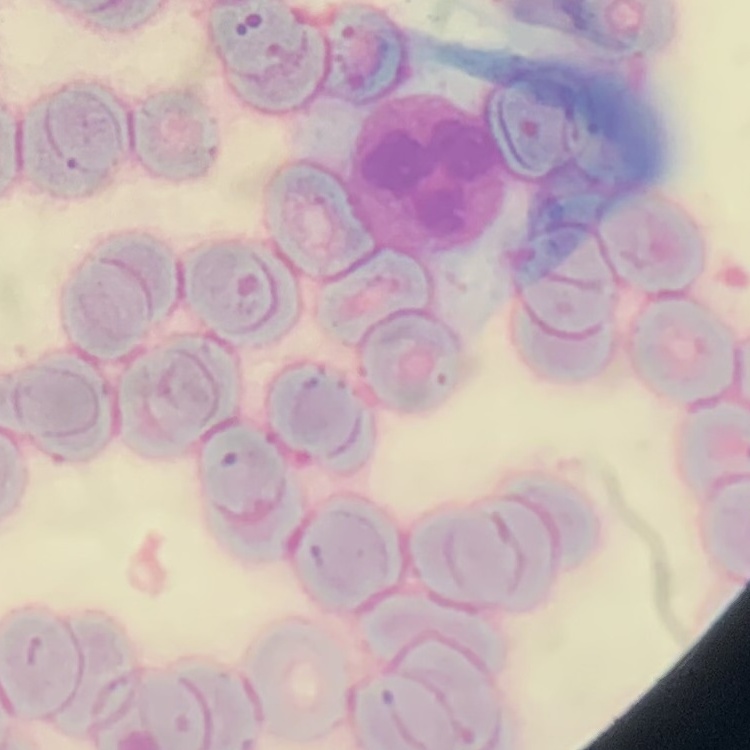
Summary:
  - Erythrocyte morphology: rouleaux formation
  - Image type: square crop of a larger photomicrograph
  - Stain: Field's or Giemsa
  - Preparation: thin blood film